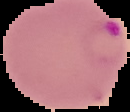
Summary:
  - Image type: segmented cell region on a black background
  - Malaria status: parasitized
  - Image size: 130×112 pixels
  - Preparation: thin blood smear